Assess the morphology of the red blood cells.
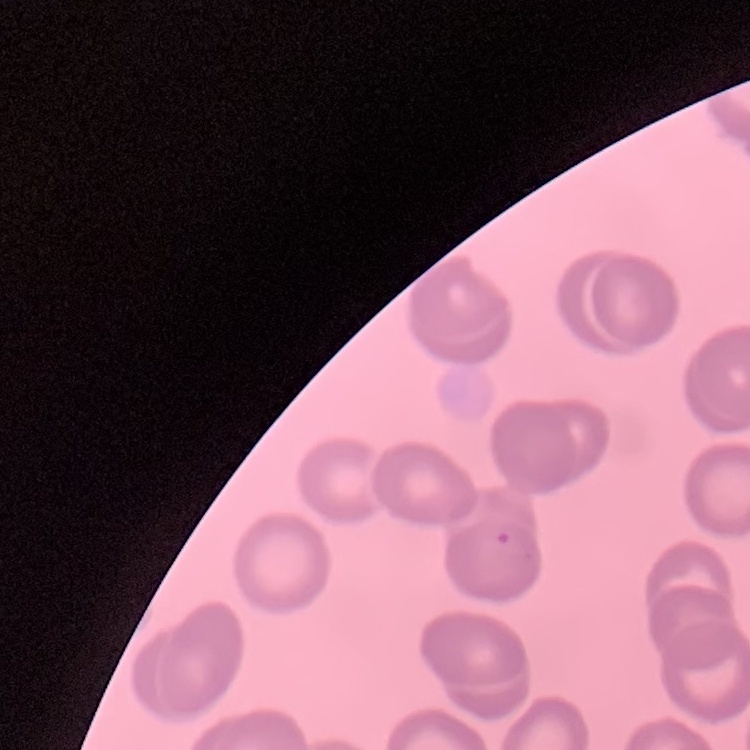
No rouleaux formation.

One tile cut from a larger photomicrograph. Thin blood film. Field's or Giemsa stain.